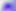

modality = photomicrograph
identification = Toxoplasma gondii
magnification = 400x